Assess this cell for malaria.
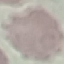
Uninfected.

stain = Giemsa
capture = smartphone camera at the microscope eyepiece
preparation = thin smear
image type = cell patch, automatically extracted from a larger field of view and resized to 64 × 64 pixels